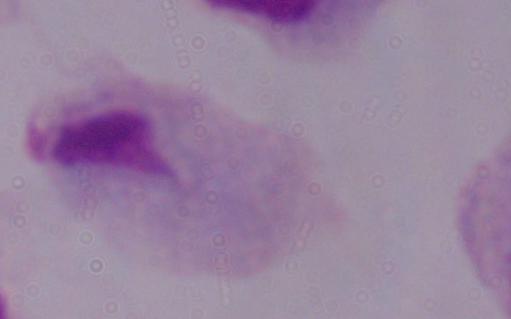
Summary:
  - Modality: photomicrograph
  - Identification: trichomonad
  - Magnification: 1000x